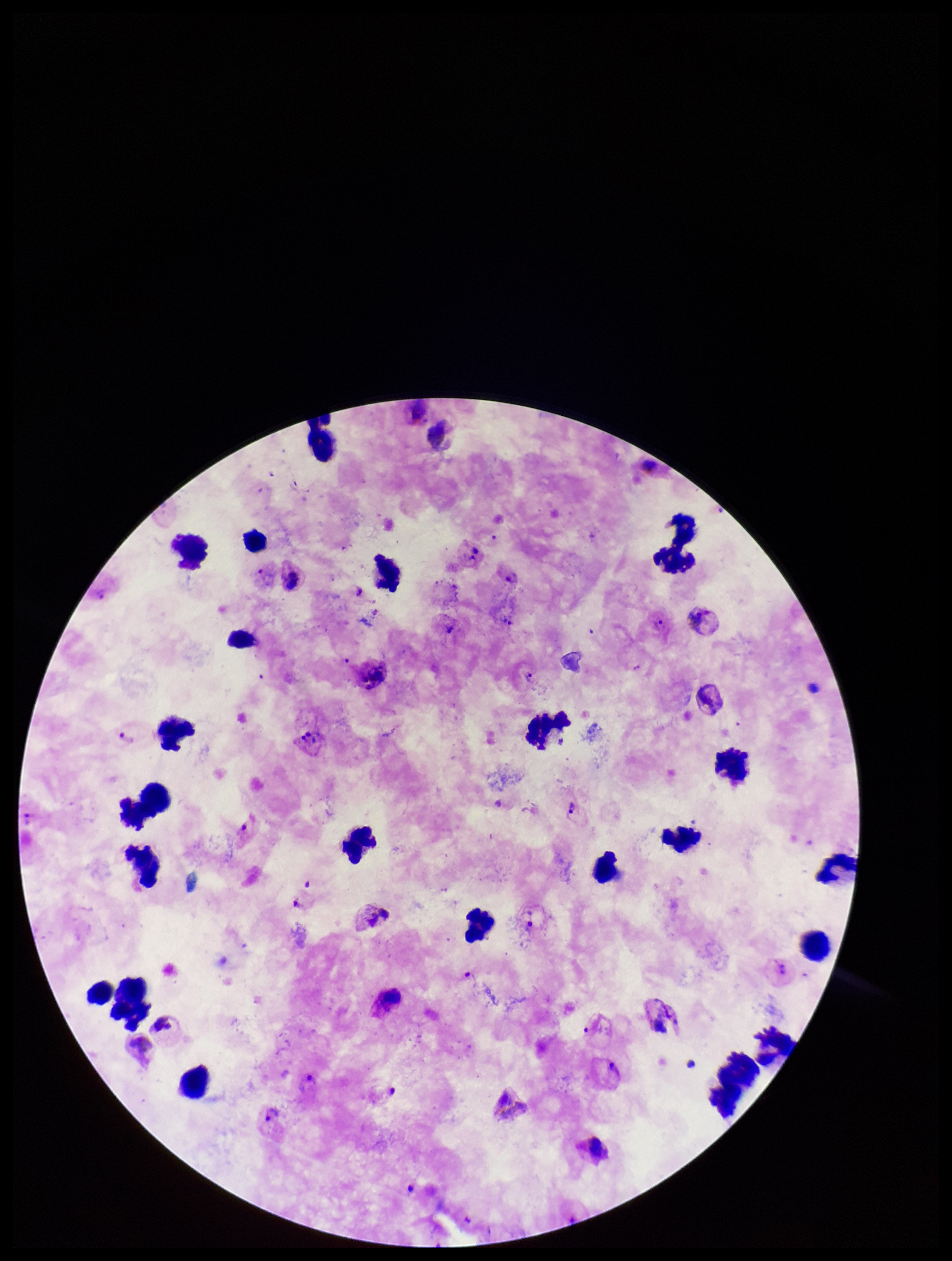

species reported for this patient = Plasmodium vivax
image size = 952×1261 pixels
capture = smartphone photograph through the microscope eyepiece
preparation = thick smear
field of view = single
leukocyte count = 26
patient malaria status = positive
parasite count = 9
Plasmodium parasites = identified
stain = Giemsa